Classify this cell by malaria status.
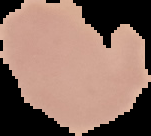
Uninfected.

image type = segmented cell region with the area outside set to black
image size = 151×136 pixels
preparation = thin blood smear